Report the malaria status of this cell.
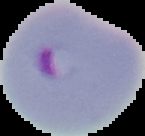
It is parasitized.

Image is 145×136 pixels. Cell region segmented out of the field of view; the surrounding area is masked to black. From a thin blood smear.